Classify this cell by malaria status.
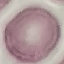

Uninfected.

Thin smear of blood. Acquired by smartphone through the microscope eyepiece. Giemsa-stained preparation. Cell patch, automatically extracted from a larger field of view and resized to 64 × 64 pixels.